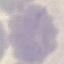 Result: no malaria parasites seen. Photographed with a smartphone camera at the microscope eyepiece. Thin smear of blood. Giemsa stain. Cell patch, automatically extracted from a larger field of view and resized to 64 × 64 pixels.